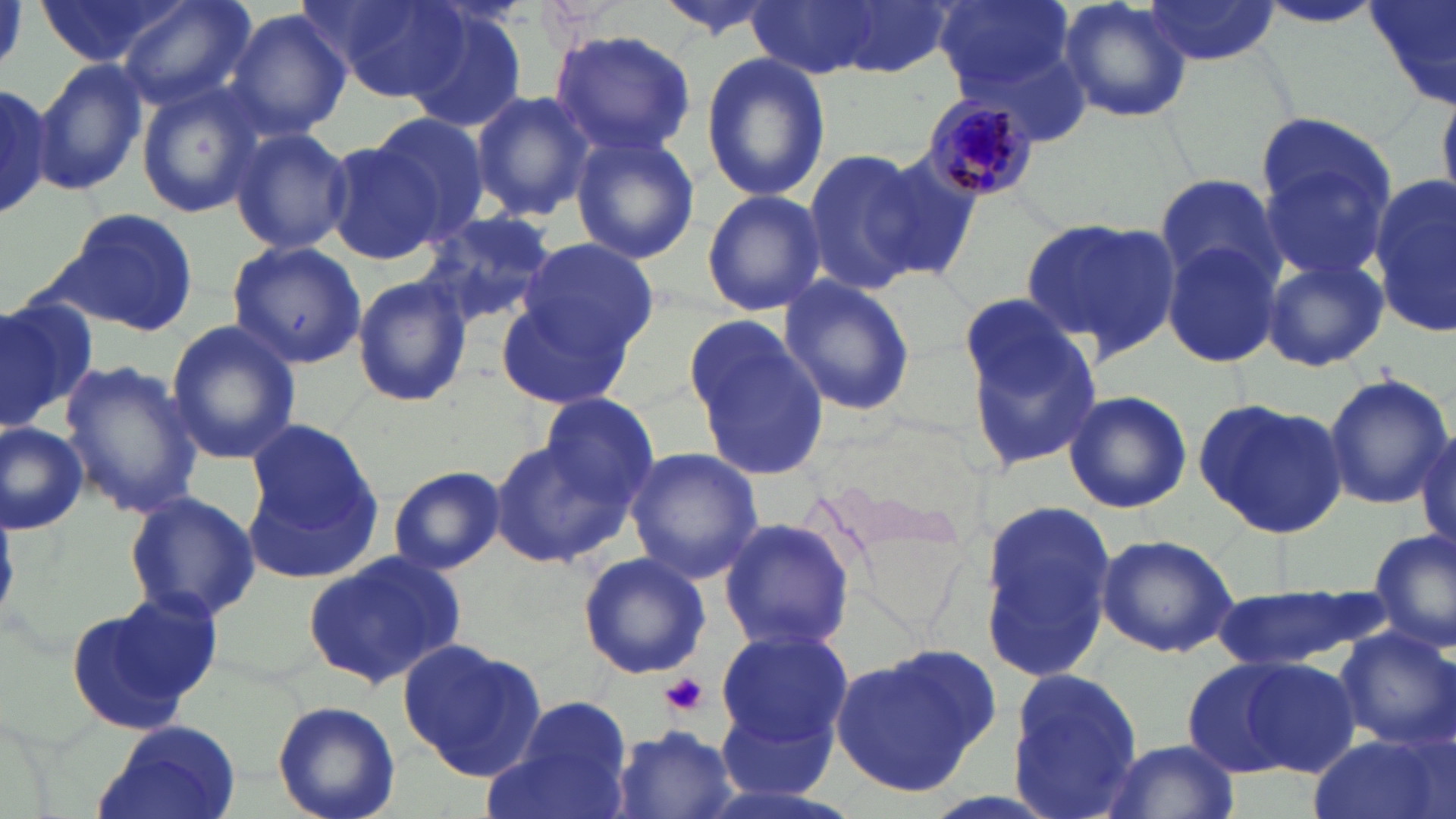 Approximate bounding boxes as [x1, y1, x2, y2] in pixels. Platelet locations: [663, 674, 708, 715]. Uninfected red blood cell locations: [39, 0, 194, 68], [115, 0, 257, 111], [317, 0, 468, 102], [652, 0, 782, 40], [745, 0, 882, 79], [827, 0, 954, 77], [935, 0, 1076, 100], [1054, 0, 1195, 126], [1144, 0, 1281, 68], [1256, 0, 1391, 30], [1363, 1, 1456, 108], [403, 6, 527, 134], [221, 8, 352, 140], [550, 29, 696, 157], [700, 52, 832, 201], [34, 56, 148, 196], [135, 81, 270, 217], [0, 84, 50, 221], [470, 89, 596, 220], [365, 112, 488, 246], [229, 126, 354, 256], [1254, 130, 1395, 279], [570, 134, 699, 266], [323, 140, 443, 264], [801, 148, 927, 294], [863, 148, 986, 281], [1153, 174, 1284, 291], [1368, 174, 1455, 332], [701, 188, 826, 317], [48, 205, 203, 336], [411, 209, 558, 328], [1020, 217, 1180, 357], [517, 236, 659, 357], [226, 238, 367, 369], [1161, 239, 1283, 370], [1261, 255, 1390, 374], [351, 275, 472, 408], [775, 275, 917, 417], [0, 291, 106, 422], [495, 293, 637, 413], [956, 294, 1102, 472], [686, 315, 830, 481], [165, 318, 300, 467], [60, 361, 203, 519], [1321, 371, 1453, 509], [1060, 389, 1193, 514], [537, 391, 664, 514], [1194, 397, 1348, 540], [0, 420, 89, 534], [245, 426, 379, 576], [1415, 427, 1454, 560], [490, 437, 632, 568], [625, 447, 765, 582], [386, 464, 506, 574], [121, 489, 261, 623], [975, 497, 1120, 683], [718, 516, 857, 653], [1367, 527, 1456, 656], [1096, 532, 1240, 657], [302, 550, 465, 691], [577, 551, 710, 680], [1211, 586, 1379, 672], [68, 589, 223, 733], [716, 623, 853, 748], [1333, 627, 1456, 750], [397, 637, 547, 780], [828, 647, 1000, 798], [1180, 654, 1331, 779], [1007, 665, 1148, 817], [719, 695, 838, 802], [495, 697, 633, 819], [271, 701, 400, 819], [94, 722, 244, 819], [611, 724, 743, 819], [1307, 732, 1449, 819], [1095, 738, 1240, 819]. Plasmodium malariae-infected red blood cell locations: [918, 93, 1044, 204]. Slide-level diagnosis: Plasmodium malariae. May-Grünwald-Giemsa-stained preparation. 1000x magnification. Single field of view. Thin blood film. Light microscopy. Image is 1456×819 pixels.